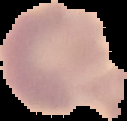 Image is 127×121 pixels. Malaria status: uninfected. Segmented cell region on a black background. From a thin blood film.